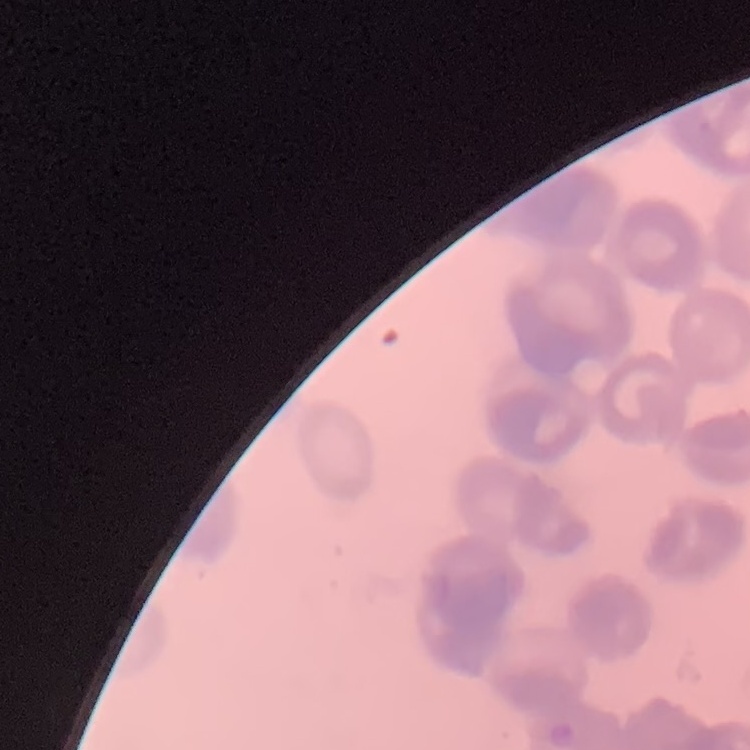
Summary:
  - Red blood cell morphology: rouleaux formation
  - Preparation: thin blood film
  - Image type: one tile cut from a larger photomicrograph
  - Stain: Field's or Giemsa